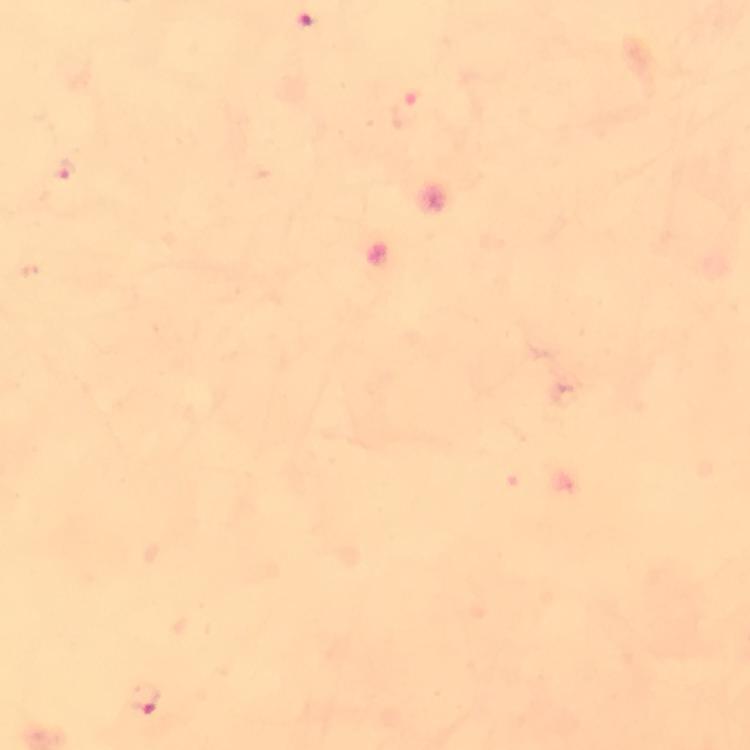

cropped from = a single field of view
context = from a malaria diagnostic workup
preparation = thick blood film
magnification = 100x
immersion oil = used
stain = Giemsa
Plasmodium parasite locations = approximate centers as [x, y] in pixels: [407, 109], [64, 170], [143, 698]
image size = 750×750 pixels
capture = smartphone camera through the microscope